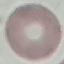
Summary:
  - Result: no malaria parasites seen
  - Capture: smartphone camera at the microscope eyepiece
  - Stain: Giemsa
  - Preparation: thin smear
  - Image type: cell patch, automatically extracted from a larger field of view and resized to 64 × 64 pixels